State which parasite is depicted.
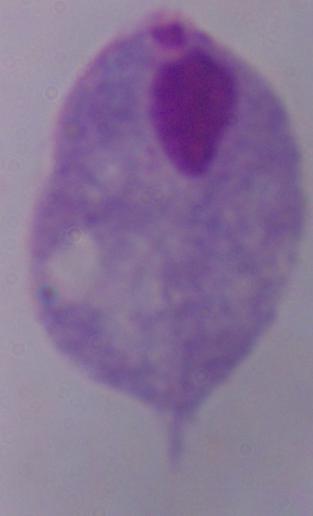

This is a trichomonad.

1000x magnification. Photomicrograph.